Locate every Plasmodium falciparum-infected red blood cell.
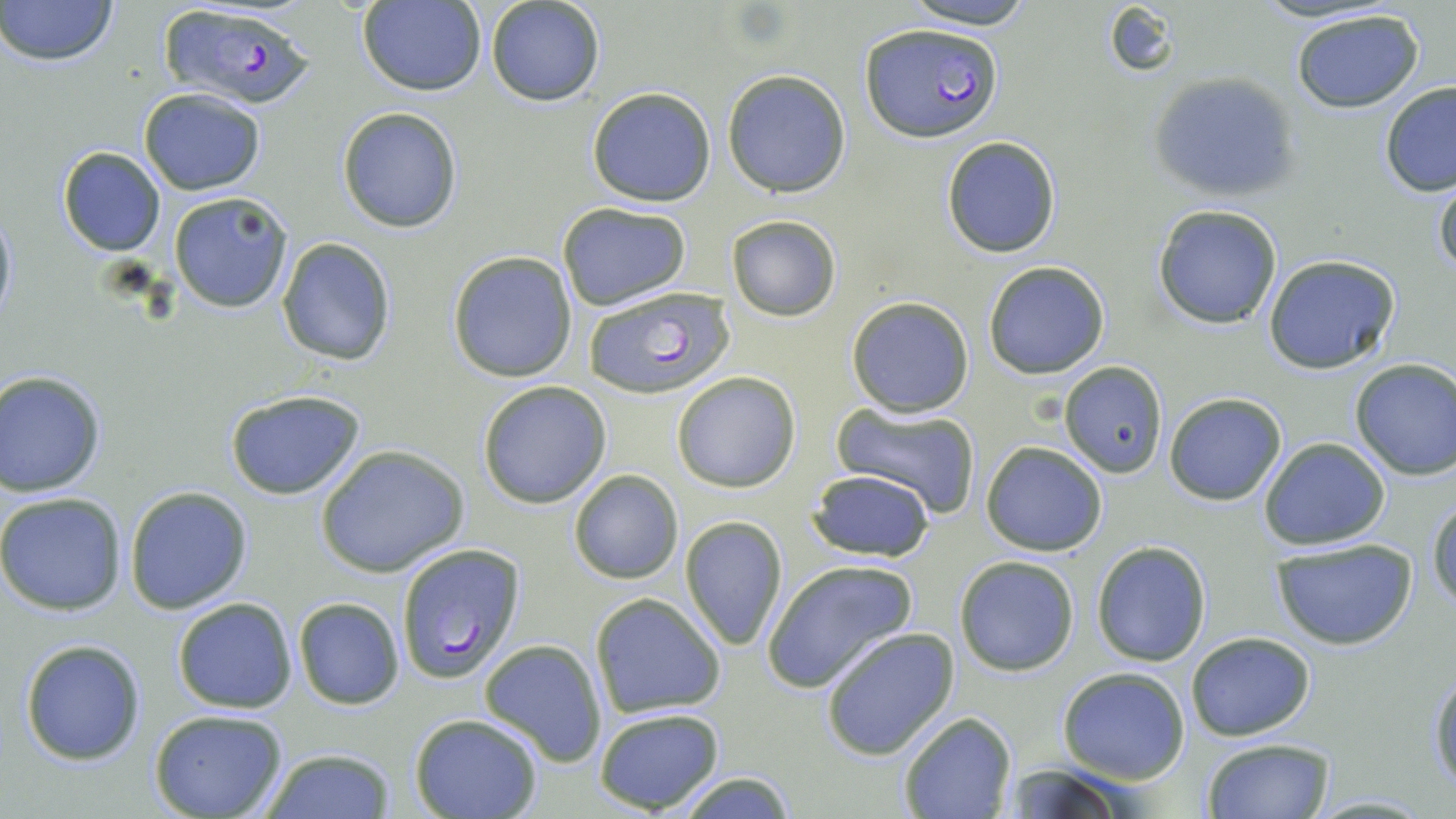

Approximate bounding boxes as [x1, y1, x2, y2] in pixels.
Plasmodium falciparum-infected red blood cells: [153, 2, 315, 106], [861, 23, 1003, 142], [581, 285, 737, 400], [393, 543, 525, 682].

Uninfected red blood cell locations: [1, 0, 120, 67], [486, 0, 606, 107], [898, 0, 1041, 30], [355, 1, 486, 95], [1100, 3, 1181, 79], [1288, 8, 1428, 112], [722, 70, 851, 198], [1150, 71, 1302, 203], [1379, 81, 1456, 197], [586, 87, 716, 207], [138, 88, 266, 194], [336, 107, 463, 233], [941, 135, 1064, 257], [57, 147, 166, 256], [1432, 171, 1455, 282], [167, 189, 294, 314], [556, 201, 694, 312], [0, 203, 17, 329], [1153, 203, 1283, 329], [726, 214, 841, 321], [276, 237, 396, 366], [447, 251, 578, 382], [1263, 253, 1400, 374], [982, 261, 1111, 380], [846, 296, 974, 418], [1347, 358, 1456, 480], [1061, 362, 1166, 478], [0, 370, 109, 498], [671, 371, 801, 493], [477, 380, 613, 508], [223, 388, 366, 501], [1163, 391, 1287, 505], [830, 400, 982, 519], [1259, 438, 1390, 550], [980, 440, 1108, 555], [315, 445, 469, 579], [568, 469, 684, 585], [805, 469, 937, 562], [124, 486, 253, 613], [0, 492, 127, 615], [1428, 496, 1456, 611], [679, 515, 789, 650], [1269, 539, 1418, 650], [1092, 541, 1212, 667], [954, 554, 1079, 676], [761, 557, 918, 691], [590, 592, 726, 718], [171, 598, 299, 714], [293, 598, 405, 710], [820, 628, 959, 760], [1185, 632, 1314, 740], [18, 637, 146, 766], [480, 638, 607, 766], [1057, 667, 1192, 783], [1428, 670, 1456, 791], [593, 707, 725, 814], [148, 709, 290, 819], [898, 710, 1016, 818], [409, 713, 544, 819], [1199, 738, 1335, 818], [257, 748, 397, 819], [999, 760, 1139, 819], [669, 770, 803, 819]. Slide-level diagnosis: Plasmodium falciparum. 1000x magnification. May-Grünwald-Giemsa stain. Thin blood film. Image is 1456×819 pixels. Light microscopy. One field of a larger specimen.